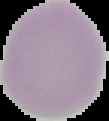

Summary:
  - Preparation: thin blood film
  - Image type: segmented cell region on a black background
  - Image size: 109×121 pixels
  - Malaria status: uninfected